Locate every Plasmodium parasite.
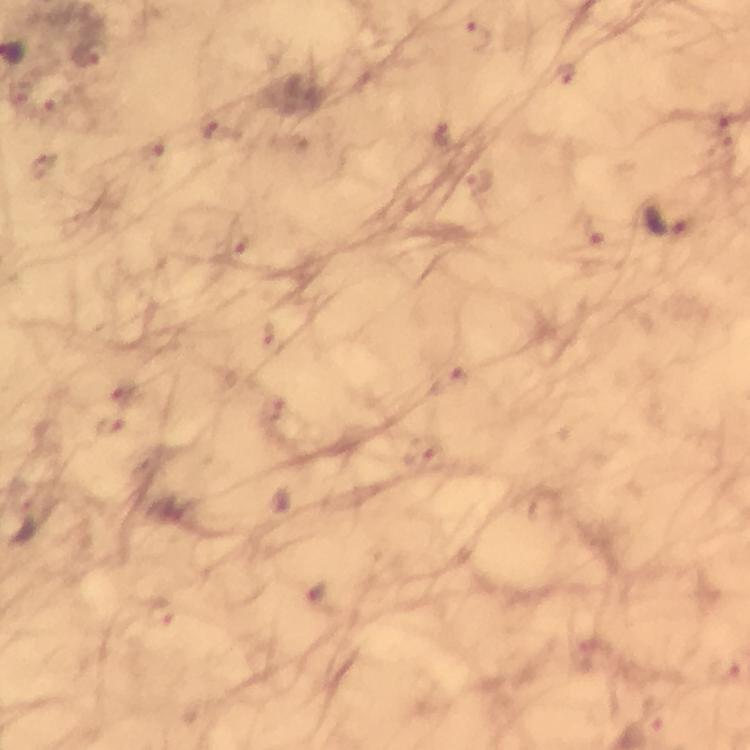
Approximate centers as (x, y) in pixels.
Plasmodium parasites: (479, 37), (565, 76), (56, 107), (218, 132), (447, 136), (153, 156), (46, 166), (479, 183), (670, 219), (587, 231), (235, 242), (269, 335), (449, 382), (124, 391), (274, 410), (110, 425), (421, 451), (30, 524), (162, 615).

Cropped region of a single field of view. Thick blood film. Photographed with a smartphone mounted on the microscope. From a diagnostic examination for malaria. Immersion oil applied. Giemsa-stained preparation. At 100x magnification. Image is 750×750 pixels.